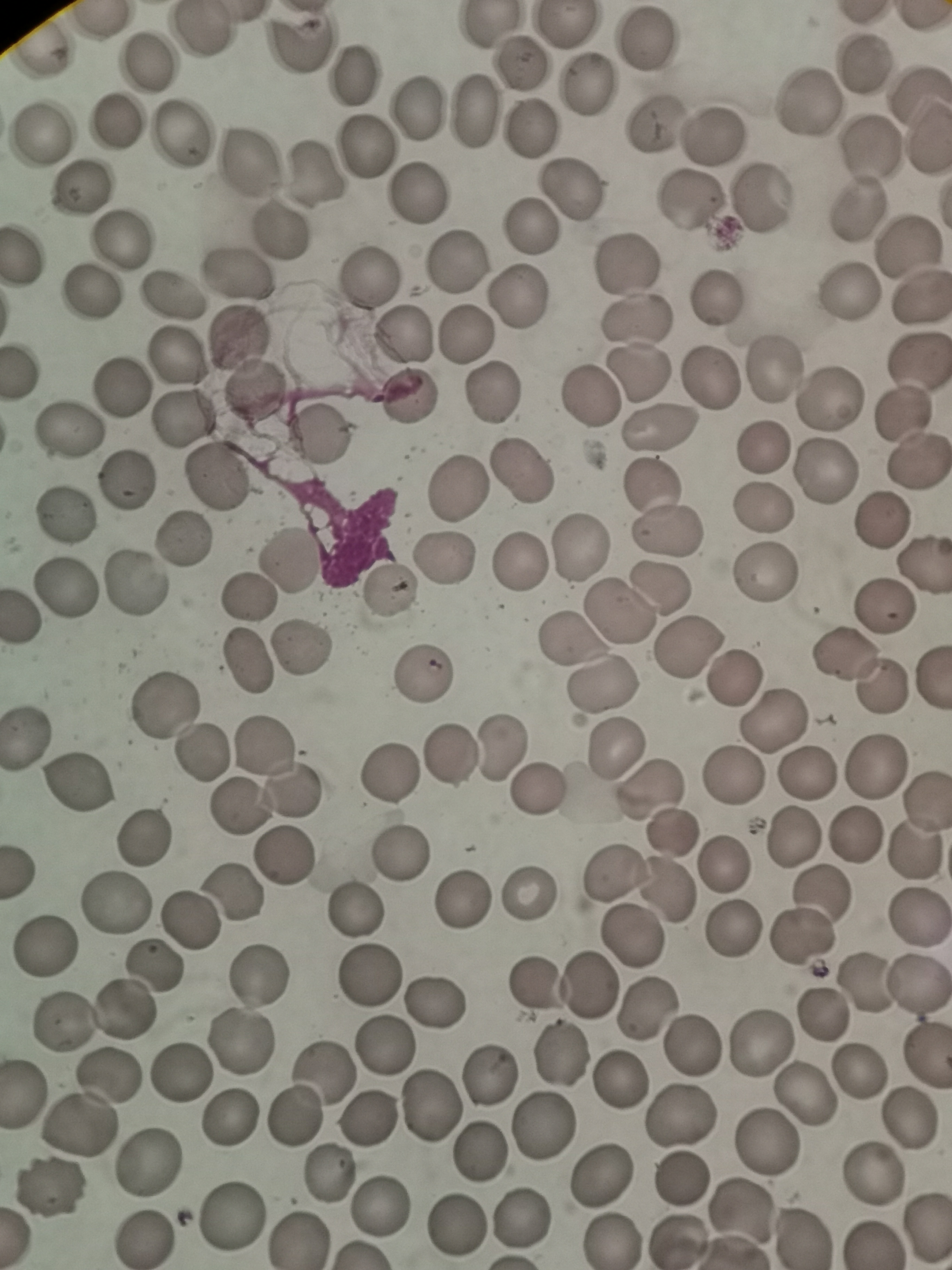
Approximate object centers, in pixels from the top-left corner.
Summary:
  - Cell locations: (x=646, y=38), (x=148, y=61), (x=861, y=62), (x=520, y=63), (x=352, y=76), (x=585, y=86), (x=808, y=102), (x=417, y=106), (x=472, y=111), (x=116, y=122), (x=654, y=122), (x=529, y=130), (x=178, y=133), (x=713, y=135), (x=40, y=137), (x=366, y=145), (x=871, y=150), (x=248, y=162), (x=314, y=172), (x=81, y=187), (x=570, y=188), (x=417, y=195), (x=760, y=200), (x=689, y=203), (x=855, y=211), (x=530, y=224), (x=280, y=232), (x=119, y=240), (x=908, y=249), (x=23, y=256), (x=458, y=260), (x=625, y=264), (x=234, y=276), (x=366, y=280), (x=88, y=292), (x=169, y=293), (x=517, y=293), (x=847, y=294), (x=717, y=297), (x=919, y=297), (x=634, y=318), (x=466, y=336), (x=238, y=339), (x=402, y=339), (x=173, y=354), (x=917, y=361), (x=776, y=369), (x=638, y=374), (x=710, y=377), (x=121, y=386), (x=254, y=391), (x=490, y=395), (x=831, y=396), (x=410, y=397), (x=586, y=400), (x=903, y=413), (x=180, y=418), (x=661, y=427), (x=68, y=434), (x=317, y=436), (x=764, y=448), (x=918, y=463), (x=520, y=471), (x=828, y=471), (x=217, y=479), (x=124, y=480), (x=651, y=486), (x=459, y=487), (x=759, y=508), (x=65, y=516), (x=881, y=520), (x=668, y=532), (x=186, y=539), (x=577, y=551), (x=447, y=557), (x=290, y=559), (x=922, y=562), (x=516, y=565), (x=762, y=572), (x=135, y=585), (x=63, y=587), (x=662, y=590), (x=390, y=591), (x=247, y=597), (x=884, y=606), (x=617, y=613), (x=22, y=617), (x=573, y=636), (x=302, y=646), (x=689, y=649), (x=845, y=656), (x=246, y=661), (x=423, y=673), (x=733, y=677), (x=603, y=684), (x=882, y=688), (x=164, y=704), (x=775, y=722), (x=26, y=735), (x=266, y=746), (x=614, y=749), (x=499, y=750), (x=202, y=753), (x=449, y=758), (x=875, y=765), (x=805, y=772), (x=387, y=773), (x=734, y=777), (x=80, y=783), (x=537, y=790), (x=652, y=792), (x=292, y=793), (x=925, y=801), (x=241, y=809), (x=673, y=831), (x=853, y=835), (x=144, y=837), (x=792, y=838), (x=398, y=853), (x=915, y=853), (x=286, y=858), (x=726, y=863), (x=614, y=875), (x=667, y=886), (x=530, y=893), (x=821, y=893), (x=233, y=895), (x=465, y=898), (x=117, y=905), (x=354, y=912), (x=920, y=919), (x=188, y=921), (x=732, y=931), (x=803, y=935), (x=634, y=937), (x=48, y=948), (x=258, y=975), (x=367, y=977), (x=537, y=983), (x=921, y=983), (x=590, y=985), (x=866, y=985), (x=435, y=1003), (x=647, y=1008), (x=824, y=1015), (x=65, y=1023), (x=238, y=1042), (x=759, y=1042), (x=690, y=1044), (x=382, y=1046), (x=926, y=1055), (x=562, y=1056), (x=178, y=1072), (x=321, y=1072), (x=860, y=1072), (x=491, y=1073), (x=111, y=1077), (x=619, y=1085), (x=22, y=1092), (x=806, y=1093), (x=429, y=1108), (x=293, y=1116), (x=682, y=1117), (x=230, y=1118), (x=910, y=1119), (x=369, y=1120), (x=544, y=1125), (x=77, y=1126), (x=767, y=1141), (x=478, y=1152), (x=148, y=1161), (x=330, y=1172), (x=602, y=1175), (x=874, y=1177), (x=683, y=1179), (x=51, y=1190), (x=379, y=1208), (x=742, y=1212), (x=231, y=1213), (x=521, y=1217), (x=459, y=1226), (x=144, y=1239), (x=299, y=1240), (x=609, y=1240), (x=675, y=1241)
  - Stain: Giemsa
  - Capture: smartphone through the microscope eyepiece
  - Field of view: single
  - Preparation: thin blood smear
  - Image size: 952×1270 pixels